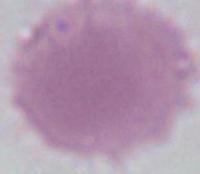

identification: erythrocyte
magnification: 1000x
modality: photomicrograph